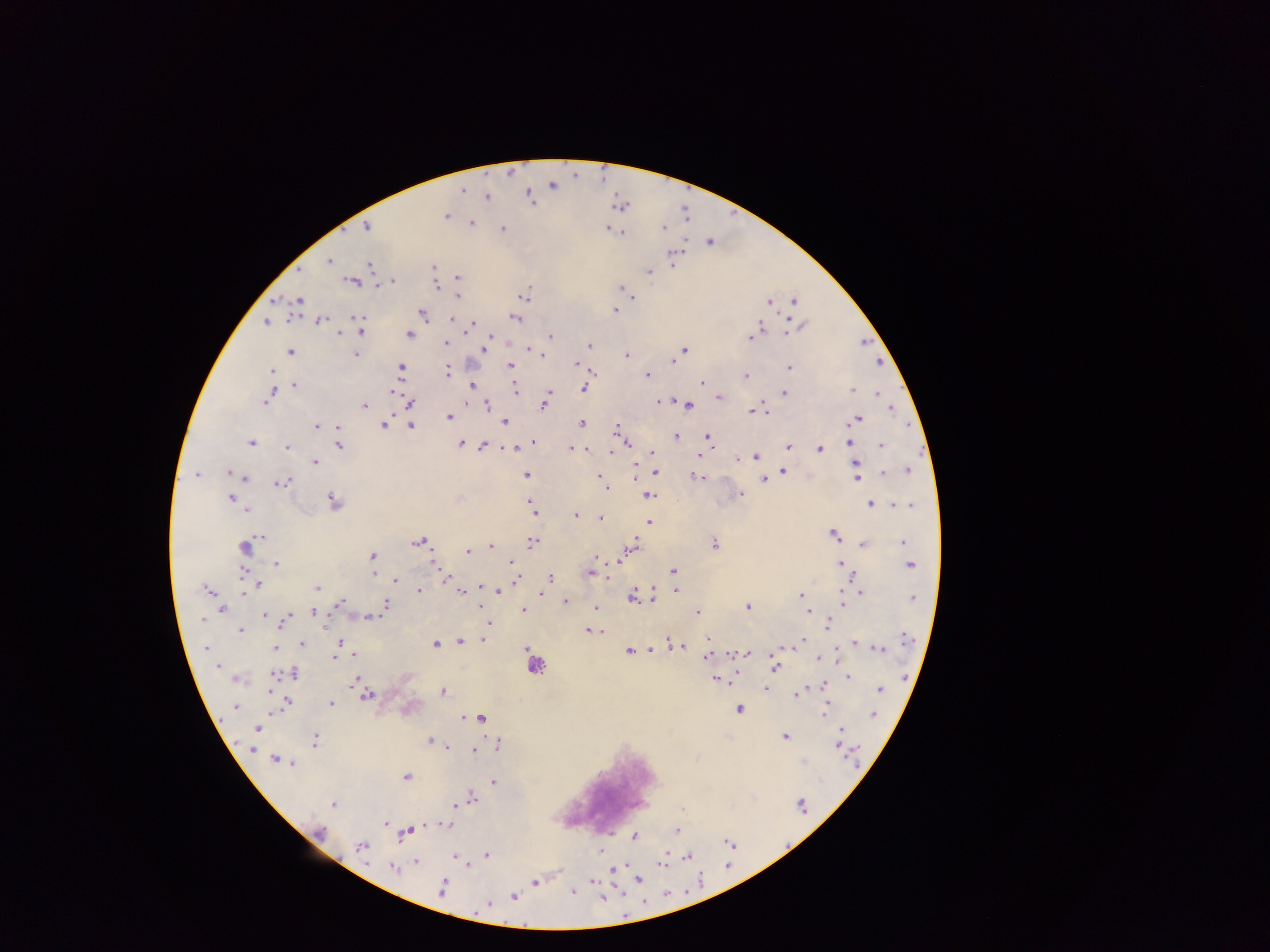

image size = 1270×952 pixels
country = Ghana
capture = mobile-phone photograph through a microscope
Plasmodium parasite locations = approximate centers as (x, y) in pixels: (553, 187), (462, 191), (529, 194), (487, 196), (620, 208), (448, 216), (472, 221), (367, 227), (502, 227), (606, 229), (623, 234), (330, 259), (369, 267), (432, 268), (649, 271), (457, 275), (393, 281), (352, 282), (436, 285), (623, 289), (627, 289), (458, 296), (631, 296), (299, 301), (795, 301), (769, 304), (614, 310), (423, 313), (358, 315), (515, 317), (320, 320), (805, 322), (266, 323), (760, 328), (361, 331), (341, 332), (790, 332), (409, 334), (361, 336), (550, 337), (489, 339), (750, 340), (447, 343), (864, 344), (590, 345), (528, 347), (533, 349), (485, 350), (685, 350), (289, 352), (627, 354), (356, 355), (541, 355), (574, 361), (671, 361), (880, 361), (278, 365), (509, 365), (401, 368), (790, 368), (273, 370), (448, 371), (591, 373), (646, 374), (747, 377), (702, 383), (296, 384), (472, 385), (514, 388), (582, 389), (515, 391), (851, 391), (857, 391), (273, 392), (551, 392), (783, 392), (393, 393), (877, 393), (269, 396), (548, 396), (719, 396), (655, 400), (266, 401), (661, 401), (688, 405), (411, 406), (487, 406), (364, 408), (544, 408), (750, 409), (894, 410), (448, 418), (859, 419), (581, 422), (505, 423), (385, 424), (411, 425), (315, 426), (336, 426), (616, 431), (619, 436), (676, 437), (709, 438), (533, 440), (848, 441), (251, 442), (461, 443), (525, 444), (484, 447), (882, 447), (339, 448), (570, 448), (788, 448), (287, 449), (513, 449), (819, 449), (575, 450), (652, 451), (614, 452), (702, 456), (756, 457), (738, 459), (314, 464), (856, 466), (636, 468), (783, 470), (910, 470), (656, 471), (228, 472), (196, 473), (527, 474), (884, 474), (697, 475), (599, 476), (635, 477), (246, 478), (764, 480), (857, 481), (285, 483), (605, 486), (607, 488), (742, 496), (331, 497), (649, 497), (230, 498), (333, 500), (528, 500), (869, 503), (896, 504), (910, 504), (534, 512), (247, 513), (576, 514), (600, 519), (649, 520), (834, 535), (262, 537), (419, 541), (532, 541), (902, 542), (714, 544), (863, 544), (491, 546), (633, 546), (245, 547), (467, 550), (372, 556), (596, 558), (620, 558), (433, 563), (513, 563), (840, 563), (275, 564), (911, 566), (673, 570), (592, 574), (373, 576), (551, 577), (395, 582), (258, 584), (479, 584), (654, 586), (318, 589), (203, 590), (208, 590), (678, 590), (419, 591), (498, 592), (861, 592), (460, 593), (541, 593), (799, 594), (842, 595), (631, 598), (655, 598), (912, 598), (566, 599), (340, 604), (385, 604), (480, 606), (842, 607), (595, 608), (749, 608), (223, 611), (524, 611), (808, 612), (696, 613), (312, 614), (264, 615), (287, 616), (369, 616), (283, 619), (201, 622), (828, 624), (488, 625), (241, 630), (588, 630), (705, 638), (803, 638), (483, 639), (461, 641), (338, 642), (853, 643), (436, 644), (304, 645), (206, 648), (275, 648), (879, 648), (629, 650), (748, 652), (777, 652), (353, 655), (708, 656), (335, 657), (819, 661), (217, 665), (774, 668), (293, 673), (281, 675), (274, 677), (356, 678), (847, 679), (714, 680), (820, 684), (824, 688), (269, 689), (766, 690), (879, 691), (443, 692), (799, 693), (269, 694), (368, 695), (289, 702), (330, 703), (826, 706), (234, 707), (739, 709), (875, 716), (481, 720), (256, 728), (841, 730), (784, 738), (314, 739), (431, 740), (437, 743), (837, 745), (449, 747), (250, 750), (473, 751), (274, 756), (293, 764), (406, 777), (493, 781), (472, 795), (334, 805), (455, 806), (385, 823), (446, 824), (421, 827), (319, 831), (677, 832), (401, 836), (636, 838), (362, 845), (600, 853), (486, 854), (416, 862), (661, 865), (393, 869), (613, 872), (639, 879), (534, 882), (593, 882), (443, 886), (573, 893), (513, 896), (487, 903)
field of view = single
preparation = thick blood film